Give the extent of all Plasmodium falciparum-infected red blood cells.
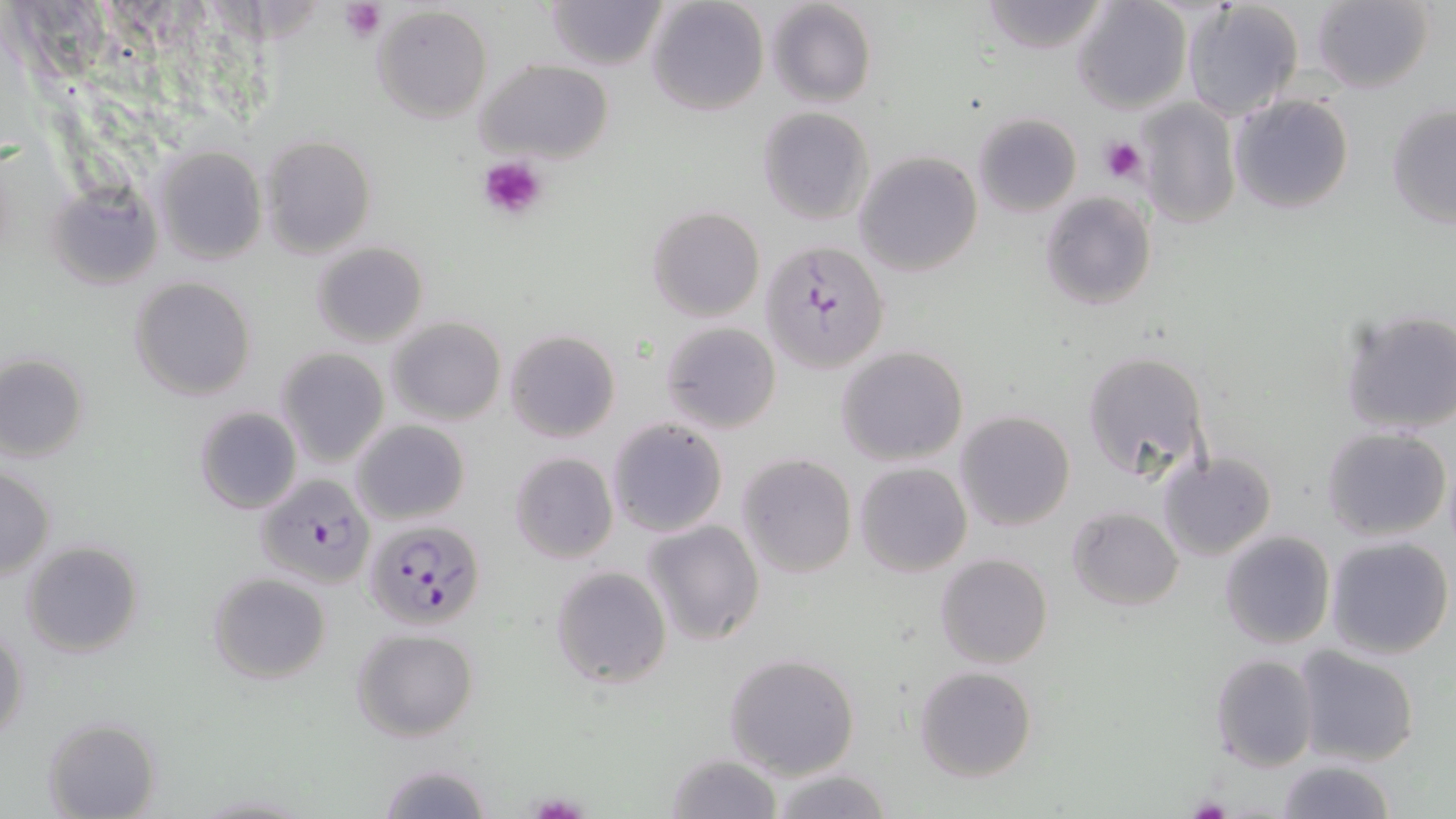

Approximate bounding boxes as (x1, y1, x2, y2) in pixels.
Plasmodium falciparum-infected red blood cells: (762, 240, 888, 373), (256, 473, 377, 589), (364, 518, 485, 630).

slide-level diagnosis = Plasmodium falciparum
field of view = one of a larger specimen
platelet locations = approximate bounding boxes as (x1, y1, x2, y2) in pixels: (339, 0, 387, 43), (1098, 136, 1148, 183), (477, 153, 547, 217), (1186, 795, 1234, 819)
magnification = 1000x
stain = May-Grünwald-Giemsa
modality = optical microscopy
image size = 1456×819 pixels
preparation = thin blood film
uninfected red blood cell locations = approximate bounding boxes as (x1, y1, x2, y2) in pixels: (546, 0, 666, 70), (645, 0, 769, 117), (767, 0, 878, 109), (979, 0, 1110, 54), (1310, 0, 1435, 94), (1073, 1, 1191, 114), (1181, 1, 1304, 121), (370, 5, 493, 124), (474, 59, 615, 163), (1229, 92, 1354, 215), (1137, 100, 1241, 230), (1386, 102, 1456, 229), (758, 107, 873, 224), (974, 112, 1081, 217), (259, 135, 376, 258), (153, 146, 266, 264), (855, 151, 983, 276), (45, 181, 161, 290), (1039, 190, 1156, 310), (646, 206, 765, 321), (312, 241, 429, 347), (129, 275, 257, 401), (1339, 307, 1456, 436), (388, 317, 505, 424), (660, 321, 782, 434), (504, 329, 620, 443), (835, 345, 968, 465), (276, 347, 390, 467), (1081, 349, 1212, 482), (0, 352, 88, 463), (194, 406, 303, 515), (955, 410, 1074, 531), (606, 418, 728, 537), (353, 419, 470, 524), (1323, 426, 1450, 541), (508, 452, 619, 565), (1159, 452, 1275, 560), (736, 453, 856, 578), (855, 463, 972, 577), (0, 466, 55, 579), (1067, 507, 1182, 610), (642, 519, 764, 646), (1218, 530, 1336, 649), (1325, 534, 1454, 660), (20, 539, 145, 659), (935, 554, 1053, 671), (550, 565, 672, 689), (207, 572, 331, 683), (1, 626, 28, 745), (351, 627, 480, 742), (1294, 645, 1421, 766), (724, 652, 859, 779), (1210, 653, 1319, 770), (915, 665, 1038, 782), (41, 717, 161, 818), (666, 753, 779, 818), (1275, 759, 1398, 818), (375, 760, 495, 818), (766, 767, 894, 819)